Outline each blood parasite and name the species.
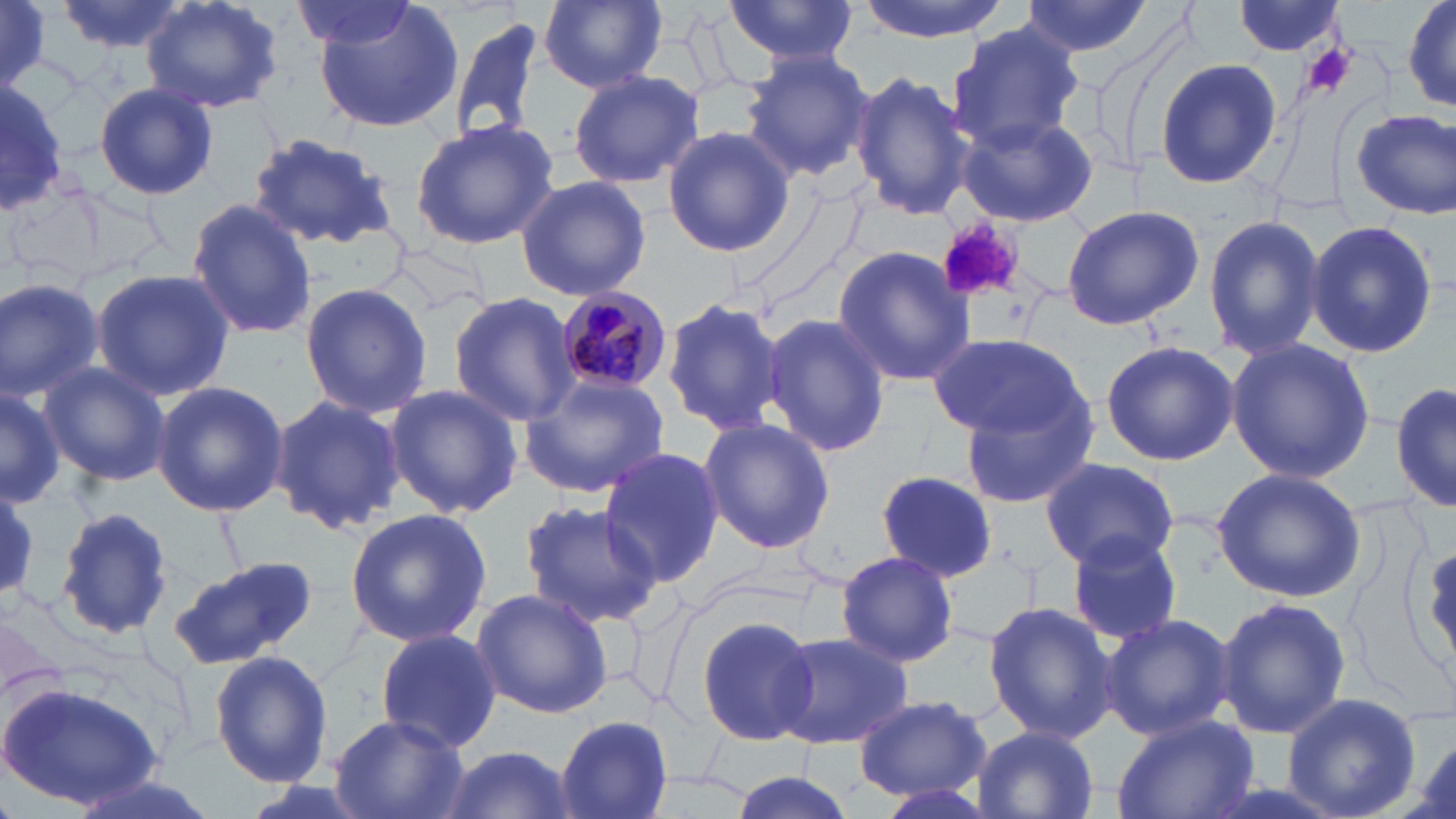
Approximate bounding boxes as (x1, y1, x2, y2) in pixels.
Plasmodium malariae-infected red blood cells: (551, 288, 671, 397).
No Plasmodium falciparum, Plasmodium ovale, Plasmodium vivax, Babesia divergens, or Trypanosoma brucei observed.

slide_level_diagnosis: Plasmodium malariae
stain: May-Grünwald-Giemsa
image_size: 1456×819 pixels
magnification: 1000x
modality: optical microscopy
uninfected_red_blood_cell_locations: 'approximate bounding boxes as (x1, y1, x2, y2) in pixels: (57, 0, 190, 54), (141, 0, 283, 114), (311, 0, 465, 134), (539, 0, 667, 91), (722, 0, 858, 67), (854, 0, 1012, 41), (1018, 0, 1157, 61), (1400, 0, 1456, 118), (0, 1, 50, 88), (289, 1, 421, 52), (1233, 2, 1349, 57), (449, 16, 543, 142), (946, 23, 1085, 152), (740, 49, 878, 180), (1154, 58, 1283, 189), (568, 69, 705, 190), (849, 71, 976, 222), (0, 83, 68, 216), (93, 83, 218, 201), (1350, 106, 1456, 220), (954, 110, 1098, 228), (409, 119, 559, 250), (663, 125, 796, 258), (246, 132, 400, 250), (515, 174, 652, 301), (185, 199, 317, 341), (1060, 202, 1204, 329), (1202, 213, 1324, 360), (1305, 219, 1439, 360), (833, 244, 977, 387), (90, 268, 235, 398), (0, 276, 104, 401), (299, 282, 433, 419), (449, 293, 582, 427), (659, 295, 787, 436), (761, 313, 890, 459), (931, 331, 1089, 442), (1226, 338, 1376, 483), (1099, 341, 1241, 465), (37, 361, 170, 486), (518, 375, 670, 499), (1392, 380, 1455, 515), (152, 381, 288, 515), (382, 384, 522, 520), (0, 385, 61, 508), (267, 393, 407, 538), (958, 395, 1099, 508), (698, 418, 835, 555), (597, 446, 725, 588), (1041, 458, 1178, 570), (1212, 467, 1365, 602), (875, 469, 1002, 580), (0, 487, 41, 597), (515, 499, 665, 629), (52, 507, 178, 643), (344, 509, 490, 648), (1066, 532, 1184, 646), (1416, 535, 1456, 683), (836, 550, 959, 668), (168, 557, 319, 670), (471, 587, 615, 720), (1214, 595, 1351, 737), (983, 601, 1117, 742), (1100, 612, 1237, 739), (694, 613, 819, 747), (375, 626, 502, 753), (769, 630, 915, 751), (209, 649, 333, 788), (1, 682, 165, 811), (1280, 692, 1424, 819), (851, 694, 991, 801), (1112, 713, 1259, 819), (329, 714, 468, 819), (556, 715, 674, 818), (969, 728, 1100, 819), (434, 744, 582, 819), (724, 769, 860, 819)'
platelet_locations: 'approximate bounding boxes as (x1, y1, x2, y2) in pixels: (1301, 45, 1359, 99), (935, 219, 1028, 306)'
field_of_view: one of a larger specimen
preparation: thin blood smear